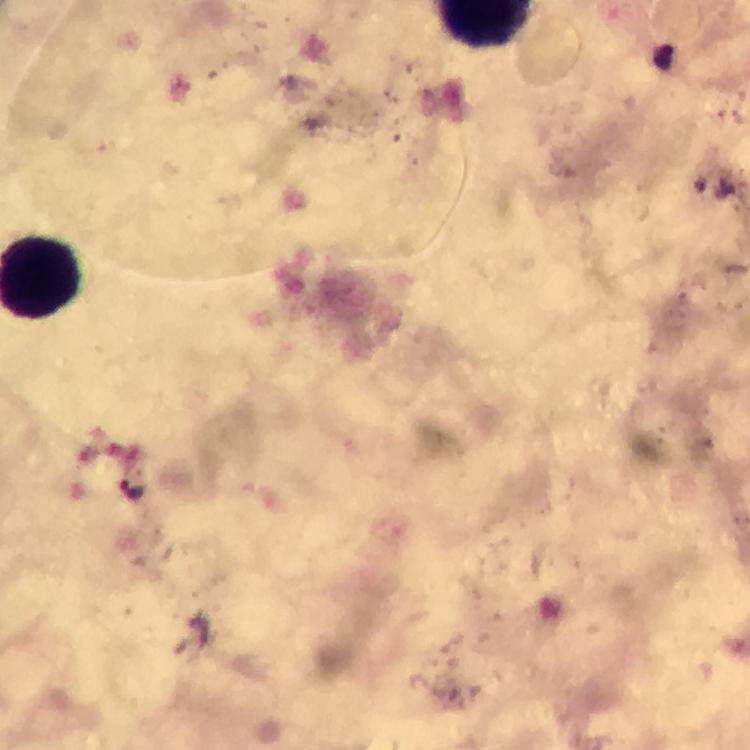
Approximate object centers, in pixels from the top-left corner. Plasmodium parasite locations: (x=134, y=490). Immersion oil was used. Image is 750×750 pixels. Smartphone photograph taken through a microscope. 100x magnification. Cropped region of a single field of view. Thick blood film. From a diagnostic examination for malaria. Giemsa-stained preparation.